Comment on the morphology of the erythrocytes.
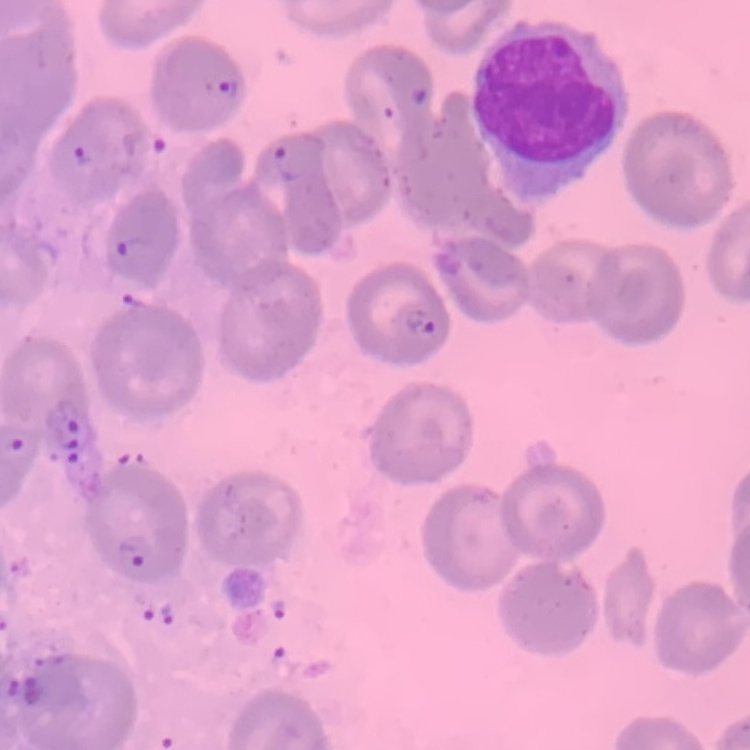
They show no rouleaux formation.

Summary:
  - Image type: one tile cut from a larger photomicrograph
  - Stain: Field's or Giemsa
  - Preparation: thin blood smear